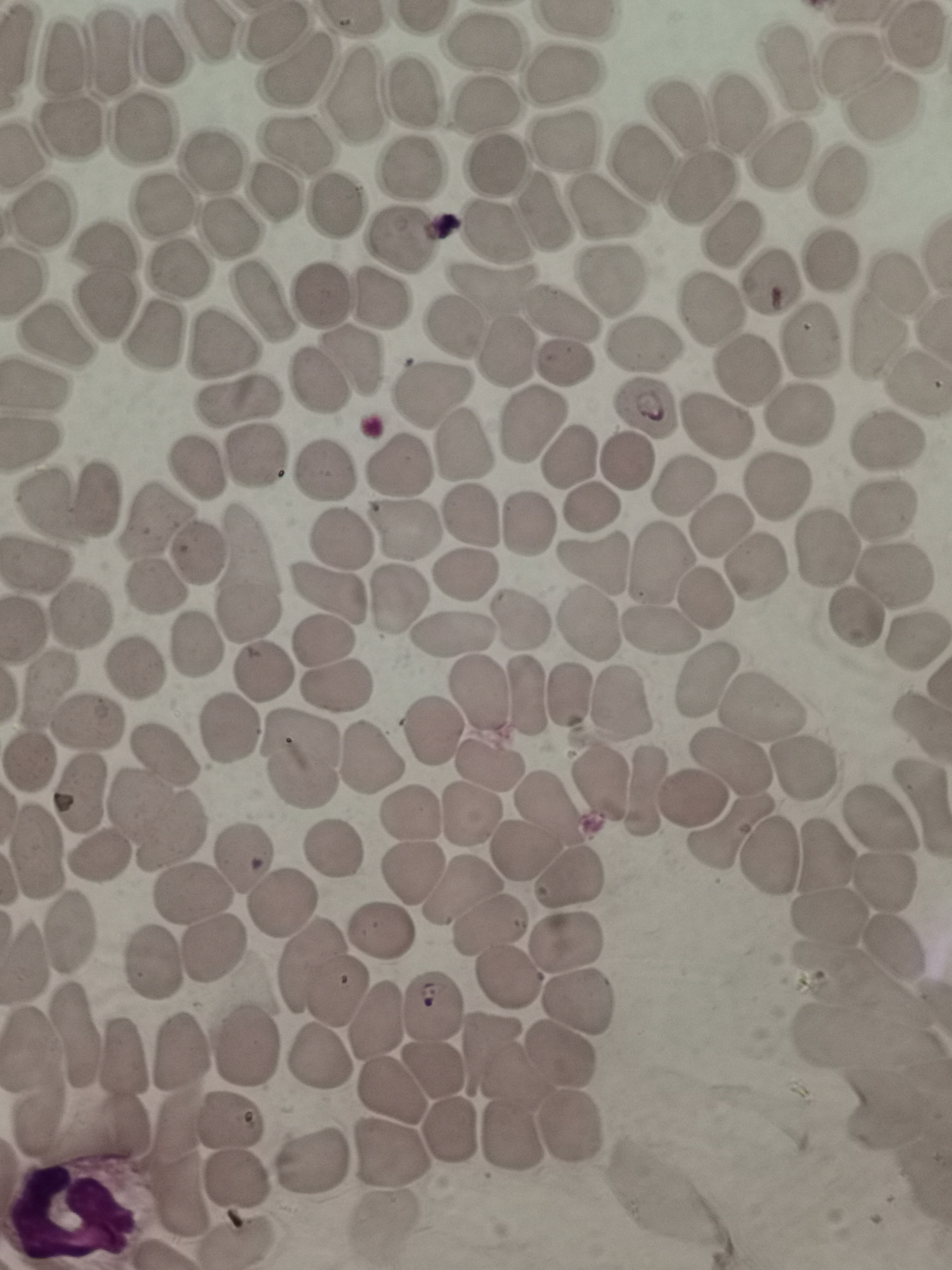
cell_locations: 'approximate centers as [x, y] in pixels: [273, 33], [484, 46], [158, 51], [63, 54], [113, 56], [299, 66], [848, 66], [783, 68], [564, 75], [414, 91], [356, 96], [488, 105], [876, 108], [738, 109], [677, 120], [74, 128], [139, 130], [564, 139], [292, 147], [782, 157], [493, 162], [213, 163], [640, 163], [408, 172], [838, 184], [701, 189], [273, 195], [338, 204], [164, 207], [603, 207], [44, 213], [542, 218], [224, 230], [728, 233], [496, 234], [403, 243], [108, 248], [832, 261], [181, 267], [609, 280], [767, 281], [899, 286], [492, 287], [317, 295], [262, 303], [378, 303], [107, 308], [710, 309], [561, 311], [452, 324], [159, 336], [55, 338], [810, 338], [643, 343], [873, 343], [224, 347], [510, 351], [353, 359], [562, 363], [747, 371], [316, 380], [916, 385], [32, 386], [432, 393], [237, 401], [647, 407], [800, 415], [530, 424], [714, 428], [885, 444], [460, 451], [260, 455], [568, 457], [627, 459], [398, 465], [196, 468], [322, 473], [683, 484], [779, 484], [97, 498], [592, 504], [50, 507], [884, 507], [468, 518], [153, 522], [720, 525], [408, 527], [527, 527], [340, 539], [825, 550], [198, 553], [596, 562], [658, 564], [37, 565], [756, 566], [246, 573], [468, 575], [895, 576], [154, 591], [706, 593], [327, 596], [398, 602], [80, 613], [857, 616], [521, 619], [589, 626], [452, 633], [656, 634], [322, 638], [917, 641], [198, 642], [134, 668], [262, 674], [708, 676], [339, 685], [47, 688], [480, 690], [570, 695], [530, 698], [621, 705], [758, 711], [88, 723], [231, 729], [435, 732], [163, 754], [372, 758], [27, 761], [302, 761], [728, 763], [488, 765], [804, 766], [596, 780], [646, 790], [78, 793], [691, 803], [550, 809], [473, 810], [922, 813], [411, 815], [160, 819], [875, 824], [729, 837], [525, 845], [333, 848], [35, 850], [94, 853], [243, 857], [768, 858], [825, 862], [412, 872], [568, 872], [886, 879], [457, 893], [195, 894], [283, 905], [832, 914], [490, 926], [71, 929], [383, 930], [569, 943], [215, 944], [898, 945], [153, 961], [323, 970], [507, 975], [579, 998], [435, 1008], [377, 1017], [75, 1033], [253, 1047], [493, 1049], [28, 1053], [183, 1053], [320, 1054], [561, 1055], [124, 1060], [428, 1070], [512, 1074], [388, 1092], [234, 1123], [571, 1123], [450, 1129], [513, 1138], [390, 1153], [316, 1162], [182, 1164], [235, 1181], [238, 1240]'
capture: smartphone camera at the microscope eyepiece
stain: Giemsa
preparation: thin smear
image_size: 952×1270 pixels
field_of_view: single